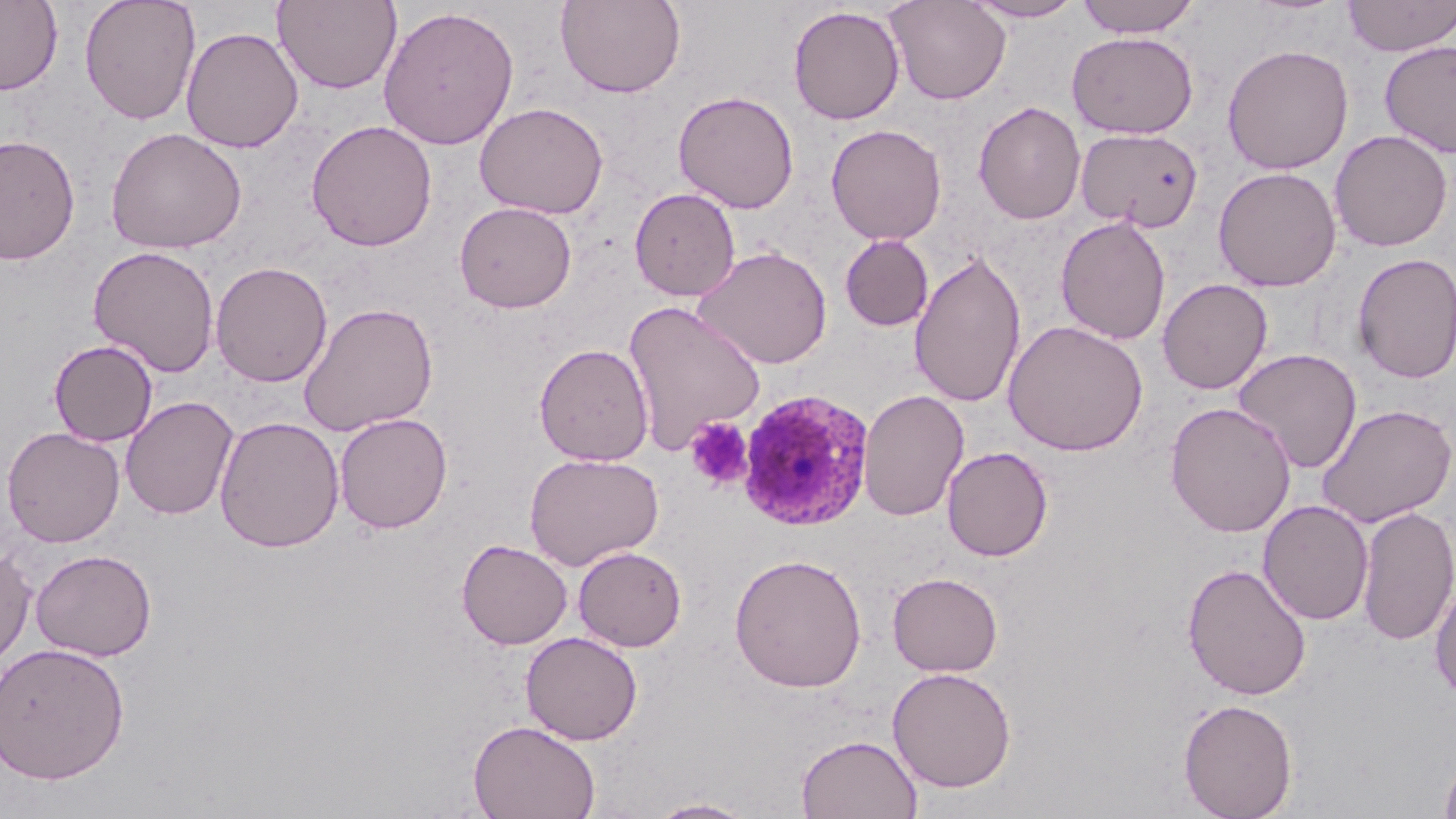

slide-level diagnosis = Plasmodium ovale
stain = May-Grünwald-Giemsa
uninfected red blood cell locations = approximate bounding boxes as (x1, y1, x2, y2) in pixels: (79, 0, 201, 125), (273, 0, 402, 93), (555, 0, 686, 98), (885, 0, 1011, 105), (965, 0, 1085, 22), (1075, 0, 1201, 38), (1342, 0, 1456, 56), (0, 1, 63, 95), (788, 5, 905, 125), (378, 6, 519, 150), (181, 26, 304, 153), (1067, 31, 1199, 139), (1380, 41, 1456, 158), (1222, 43, 1354, 175), (673, 90, 799, 214), (973, 101, 1086, 225), (474, 102, 609, 219), (306, 120, 437, 252), (825, 124, 947, 245), (106, 127, 247, 254), (1075, 127, 1204, 232), (1329, 130, 1453, 252), (0, 134, 80, 264), (1212, 166, 1342, 292), (629, 187, 741, 301), (454, 201, 577, 314), (1055, 215, 1172, 345), (839, 234, 934, 331), (88, 245, 220, 377), (693, 245, 832, 370), (909, 248, 1026, 410), (1352, 252, 1456, 384), (210, 261, 332, 387), (1157, 278, 1272, 395), (299, 302, 438, 436), (623, 302, 765, 455), (1003, 320, 1148, 456), (48, 339, 158, 446), (533, 343, 654, 466), (1231, 348, 1362, 474), (858, 389, 970, 522), (120, 396, 239, 520), (1165, 401, 1297, 537), (1317, 403, 1455, 528), (334, 412, 453, 533), (214, 416, 345, 553), (1, 426, 125, 547), (942, 446, 1053, 561), (524, 453, 663, 571), (1258, 500, 1374, 625), (1357, 507, 1456, 646), (457, 539, 573, 650), (573, 545, 687, 652), (0, 546, 36, 669), (30, 548, 156, 661), (729, 553, 867, 693), (1182, 562, 1312, 701), (887, 572, 1003, 677), (1429, 579, 1456, 703), (520, 631, 643, 745), (0, 641, 130, 785), (887, 666, 1017, 793), (1178, 698, 1298, 819), (468, 719, 600, 819), (796, 734, 922, 819), (1439, 745, 1456, 819), (645, 797, 759, 818)
modality = light microscopy
Plasmodium ovale-infected red blood cell locations = approximate bounding boxes as (x1, y1, x2, y2) in pixels: (737, 388, 874, 531)
image size = 1456×819 pixels
platelet locations = approximate bounding boxes as (x1, y1, x2, y2) in pixels: (684, 417, 754, 491)
preparation = thin blood film
magnification = 1000x
field of view = single